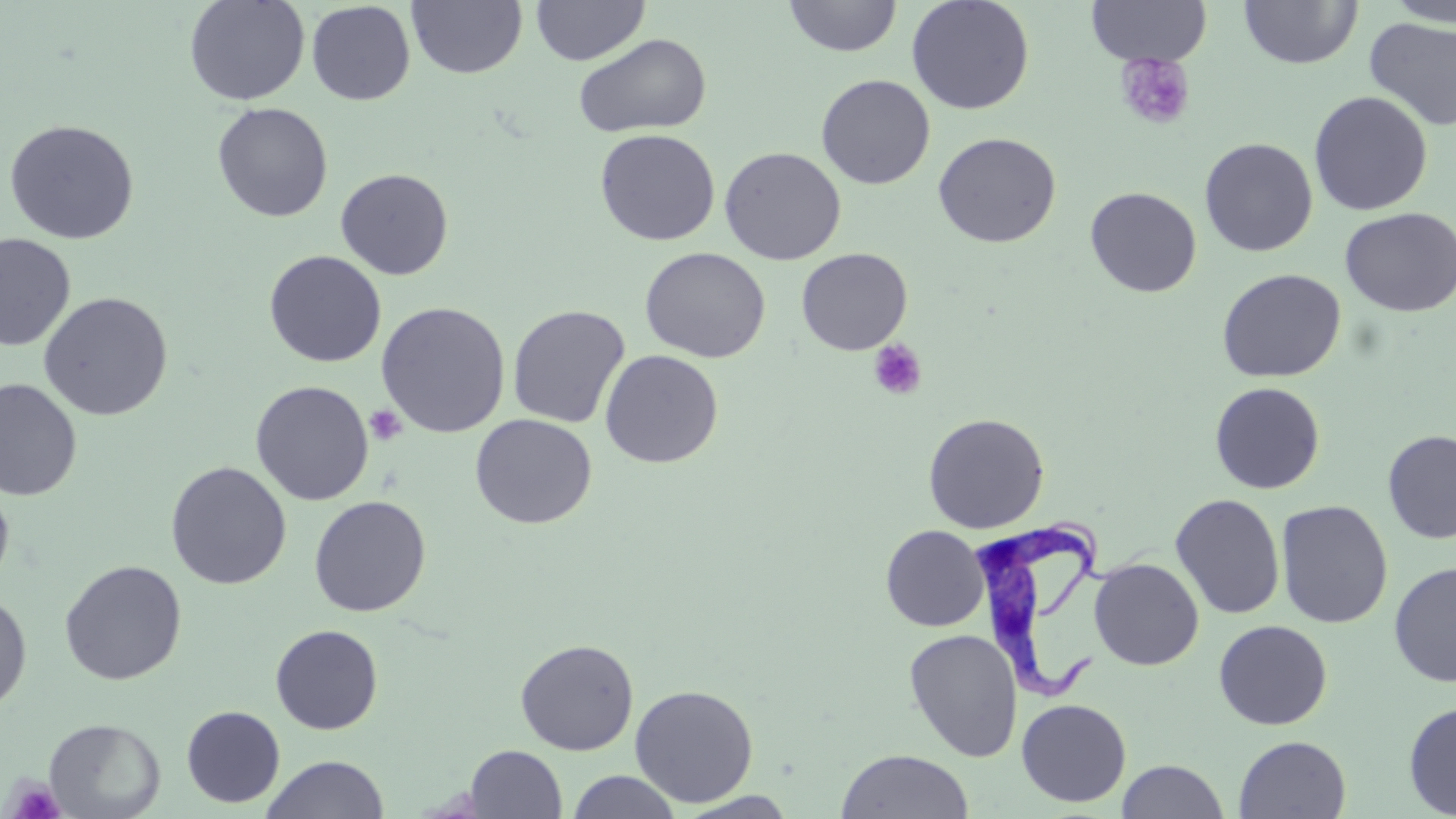

Summary:
  - Coordinate format: approximate bounding boxes as (x1, y1, x2, y2) in pixels
  - Trypanosoma brucei locations: (971, 506, 1110, 702)
  - Uninfected red blood cell locations: (184, 0, 311, 106), (530, 0, 650, 65), (783, 0, 902, 57), (906, 0, 1035, 115), (1086, 0, 1211, 66), (1382, 0, 1456, 27), (306, 1, 415, 105), (407, 1, 528, 80), (1239, 1, 1362, 69), (1364, 18, 1456, 132), (573, 33, 712, 138), (815, 74, 936, 190), (1308, 90, 1433, 216), (212, 102, 333, 223), (3, 118, 140, 245), (595, 129, 720, 246), (933, 132, 1061, 248), (1199, 137, 1318, 257), (719, 146, 846, 265), (335, 168, 454, 280), (1084, 186, 1202, 297), (1339, 207, 1456, 317), (1, 233, 75, 351), (639, 247, 771, 363), (796, 248, 912, 355), (264, 250, 386, 368), (1217, 268, 1346, 383), (38, 291, 174, 421), (376, 301, 510, 438), (507, 305, 630, 428), (600, 350, 723, 468), (0, 379, 82, 502), (250, 380, 374, 505), (1209, 382, 1325, 494), (923, 412, 1049, 534), (470, 414, 597, 529), (1382, 430, 1456, 543), (166, 461, 291, 590), (0, 480, 15, 595), (1170, 493, 1285, 619), (308, 495, 431, 617), (1275, 499, 1393, 629), (881, 525, 989, 631), (1089, 558, 1204, 670), (59, 560, 187, 685), (1388, 562, 1456, 688), (0, 590, 33, 713), (1213, 620, 1332, 730), (270, 624, 383, 734), (904, 629, 1023, 762), (515, 638, 639, 755), (629, 684, 759, 808), (1016, 698, 1131, 807), (1403, 701, 1456, 817), (181, 705, 285, 808), (43, 717, 166, 818), (1233, 735, 1351, 818), (465, 745, 567, 818), (836, 750, 974, 818), (261, 754, 389, 818), (1116, 760, 1229, 818), (566, 770, 682, 818), (675, 791, 801, 818)
  - Platelet locations: (1114, 54, 1195, 130), (868, 339, 927, 400), (365, 404, 407, 446), (5, 775, 67, 818)
  - Slide-level diagnosis: Trypanosoma brucei
  - Image size: 1456×819 pixels
  - Modality: optical microscopy
  - Preparation: thin blood film
  - Magnification: 1000x
  - Field of view: single
  - Stain: May-Grünwald-Giemsa